Locate and identify every blood parasite.
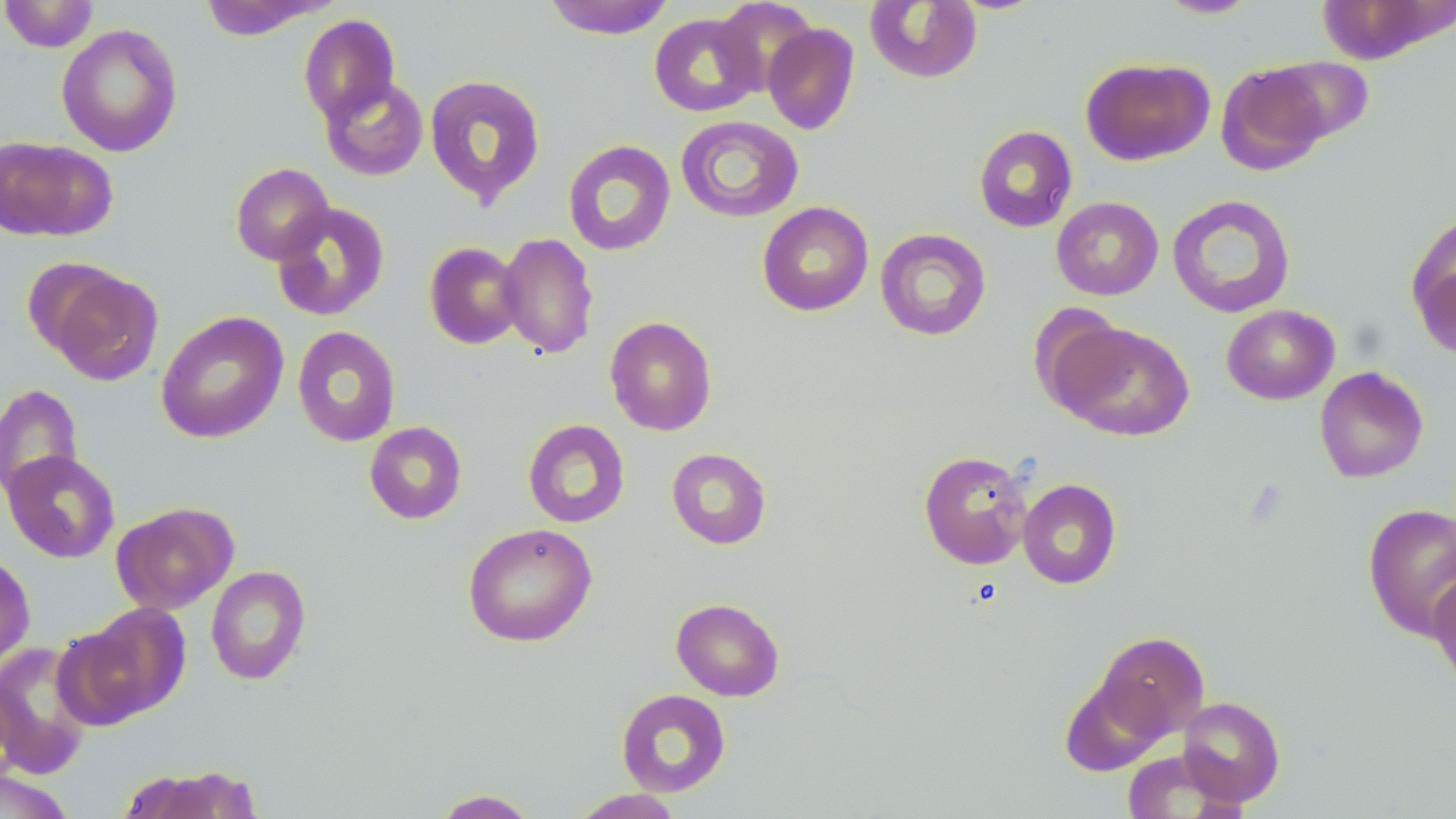

No blood parasites observed.

Summary:
  - Coordinate format: approximate bounding boxes as named x1/y1/x2/y2 corners in pixels
  - Uninfected red blood cell locations: (x1=0, y1=0, x2=98, y2=53), (x1=542, y1=0, x2=674, y2=39), (x1=865, y1=0, x2=982, y2=84), (x1=1156, y1=0, x2=1259, y2=19), (x1=199, y1=1, x2=332, y2=41), (x1=713, y1=1, x2=817, y2=96), (x1=648, y1=12, x2=763, y2=117), (x1=298, y1=14, x2=401, y2=124), (x1=763, y1=23, x2=860, y2=135), (x1=57, y1=24, x2=183, y2=157), (x1=1262, y1=55, x2=1374, y2=145), (x1=1081, y1=57, x2=1214, y2=166), (x1=1216, y1=62, x2=1331, y2=174), (x1=424, y1=74, x2=546, y2=207), (x1=320, y1=76, x2=429, y2=181), (x1=675, y1=115, x2=804, y2=223), (x1=973, y1=125, x2=1077, y2=233), (x1=0, y1=136, x2=117, y2=242), (x1=562, y1=140, x2=676, y2=256), (x1=230, y1=162, x2=334, y2=265), (x1=1167, y1=194, x2=1296, y2=318), (x1=1051, y1=196, x2=1164, y2=300), (x1=756, y1=201, x2=874, y2=317), (x1=271, y1=202, x2=390, y2=322), (x1=1408, y1=218, x2=1456, y2=357), (x1=875, y1=228, x2=991, y2=341), (x1=497, y1=232, x2=599, y2=359), (x1=424, y1=242, x2=525, y2=349), (x1=45, y1=268, x2=163, y2=386), (x1=1028, y1=303, x2=1129, y2=415), (x1=1221, y1=304, x2=1340, y2=405), (x1=156, y1=311, x2=289, y2=443), (x1=604, y1=316, x2=717, y2=436), (x1=1053, y1=321, x2=1195, y2=441), (x1=292, y1=326, x2=401, y2=447), (x1=1315, y1=366, x2=1429, y2=483), (x1=0, y1=383, x2=83, y2=503), (x1=523, y1=419, x2=630, y2=528), (x1=364, y1=421, x2=467, y2=525), (x1=666, y1=447, x2=772, y2=549), (x1=918, y1=449, x2=1032, y2=570), (x1=2, y1=450, x2=120, y2=563), (x1=1018, y1=478, x2=1121, y2=589), (x1=111, y1=502, x2=238, y2=614), (x1=1363, y1=504, x2=1456, y2=641), (x1=462, y1=522, x2=597, y2=647), (x1=0, y1=552, x2=36, y2=674), (x1=205, y1=565, x2=311, y2=685), (x1=1428, y1=569, x2=1456, y2=693), (x1=670, y1=597, x2=785, y2=701), (x1=60, y1=605, x2=188, y2=727), (x1=1094, y1=631, x2=1209, y2=740), (x1=0, y1=641, x2=95, y2=779), (x1=1060, y1=675, x2=1169, y2=777), (x1=616, y1=689, x2=731, y2=797), (x1=1177, y1=696, x2=1285, y2=807), (x1=1121, y1=749, x2=1242, y2=818), (x1=115, y1=764, x2=262, y2=818), (x1=0, y1=768, x2=78, y2=819), (x1=431, y1=788, x2=541, y2=818), (x1=568, y1=788, x2=685, y2=818)
  - Slide-level diagnosis: no evidence of blood parasites
  - Image size: 1456×819 pixels
  - Field of view: single
  - Stain: May-Grünwald-Giemsa
  - Magnification: 1000x
  - Modality: light microscopy
  - Preparation: thin blood smear